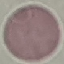
{
  "result": "negative for malaria parasites",
  "preparation": "thin smear",
  "stain": "Giemsa",
  "image_type": "cell patch, automatically extracted from a larger field of view and resized to 64 × 64 pixels",
  "capture": "smartphone through the microscope eyepiece"
}